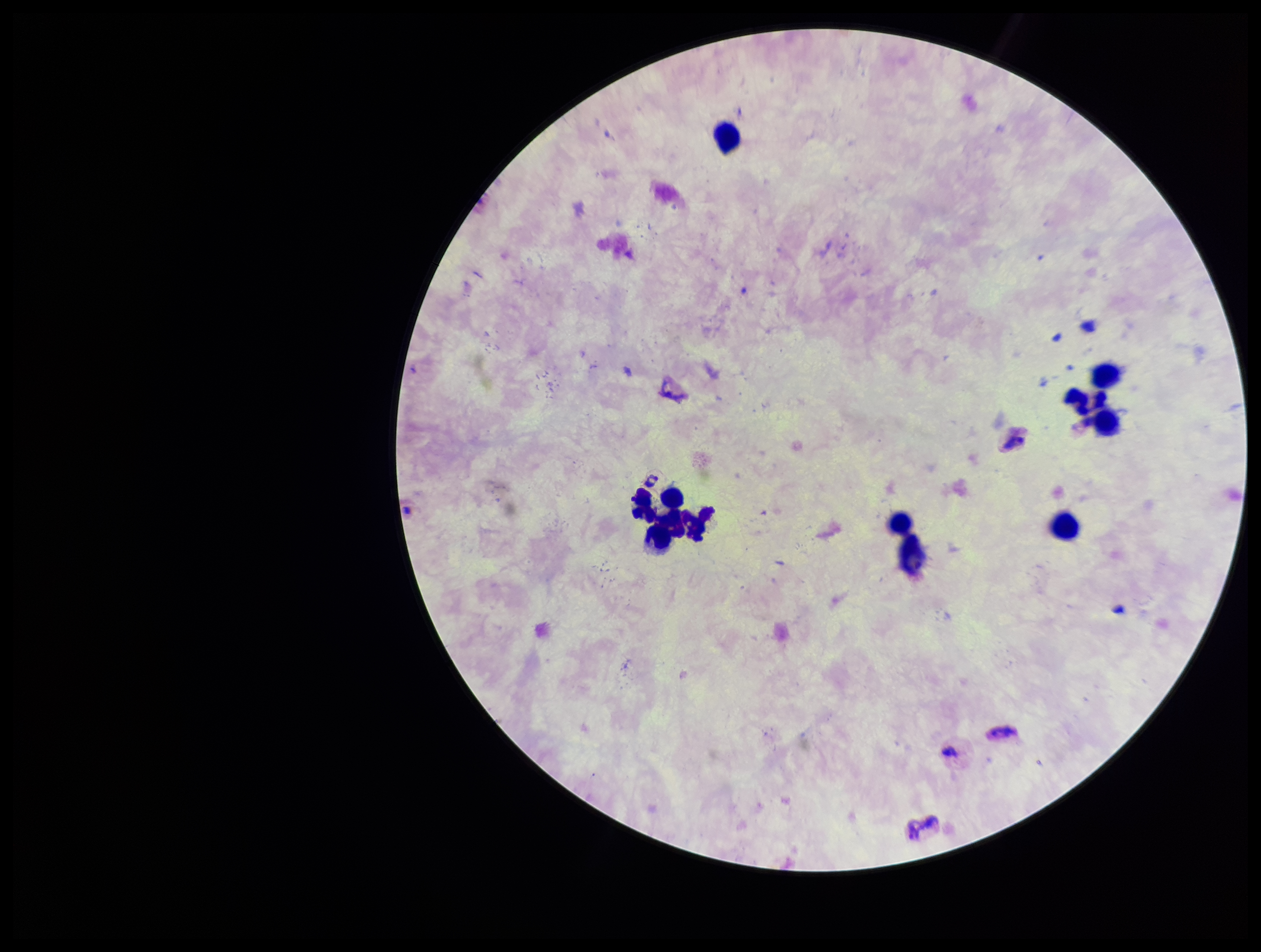 Preparation: thick blood smear. Giemsa stain. Parasite count: 0. Plasmodium parasites: none identified. Image is 1261×952 pixels. Photographed through the microscope eyepiece with a smartphone camera. Patient malaria status: infected. Leukocyte count: 11. Single field of view. Species reported for this patient: Plasmodium vivax.